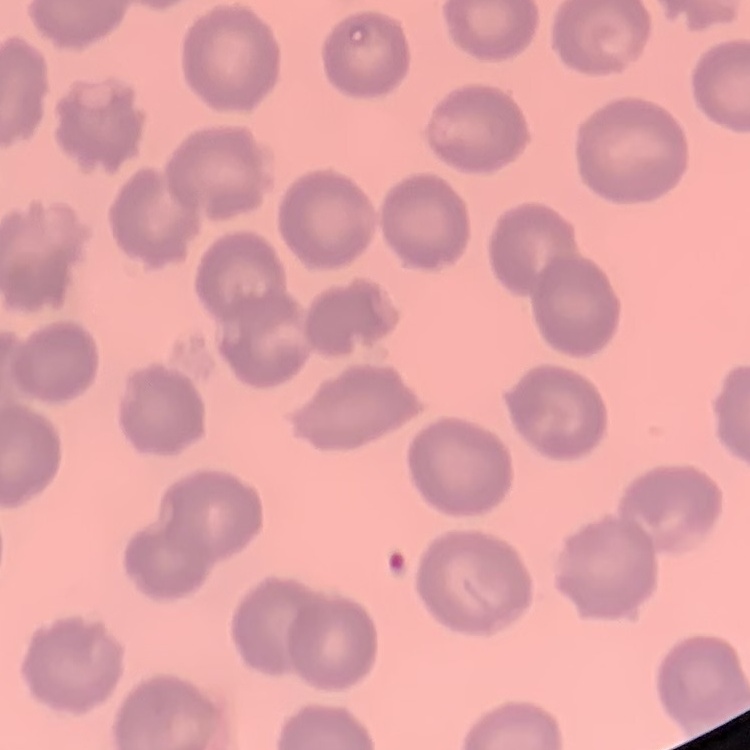

erythrocyte morphology = no rouleaux formation
stain = Field's or Giemsa
preparation = thin blood film
image type = square crop of a larger photomicrograph